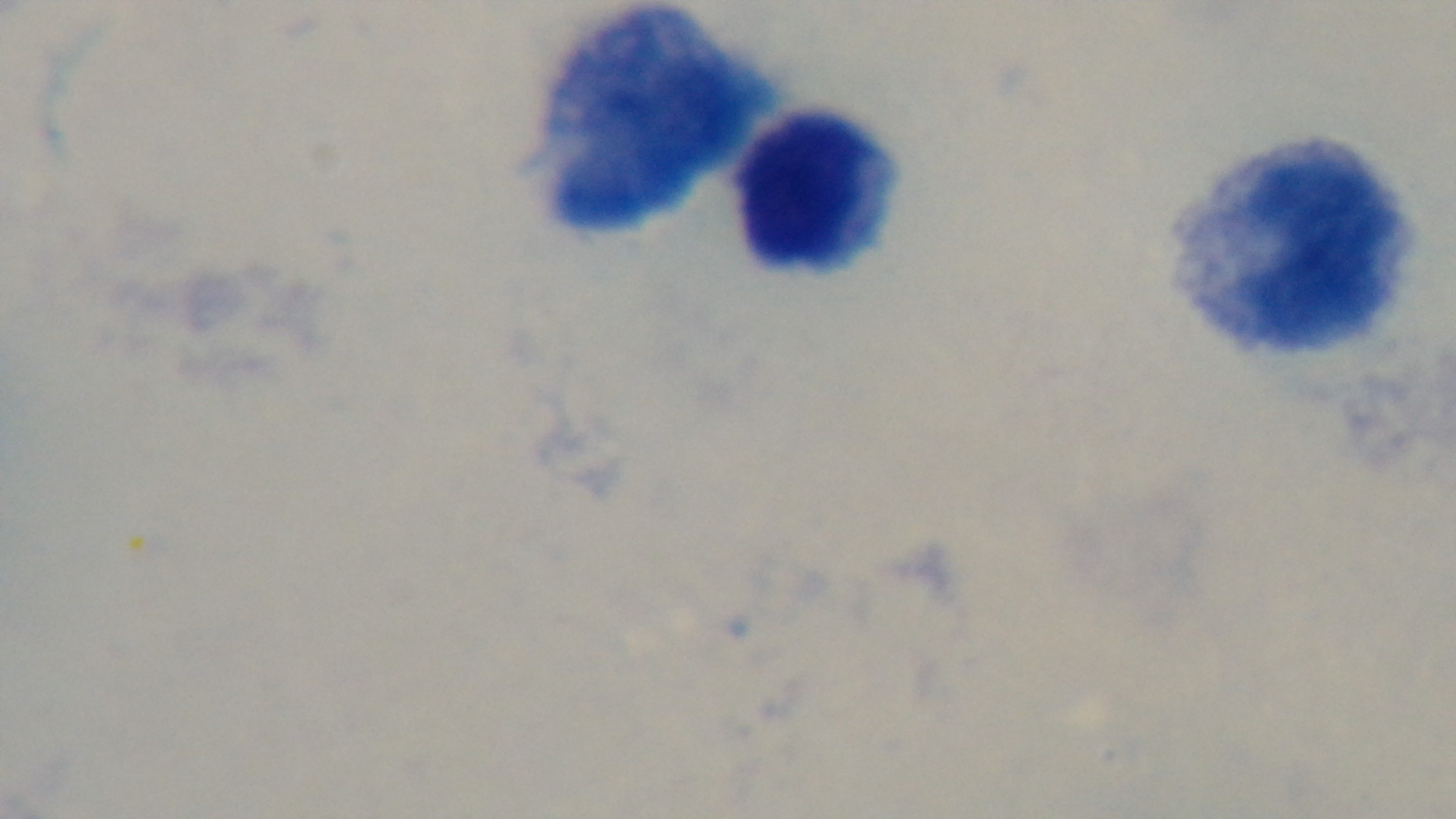

Preparation: thick smear. One field from the slide. Giemsa-stained. Malaria status: negative. Captured with a mounted 4K digital camera. Light microscopy. Oil-immersion objective, 100x.